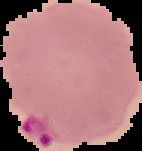

Summary:
  - Preparation: thin blood smear
  - Malaria status: parasitized
  - Image size: 142×151 pixels
  - Image type: segmented cell region on a black background